Give a bounding box for every trophozoite.
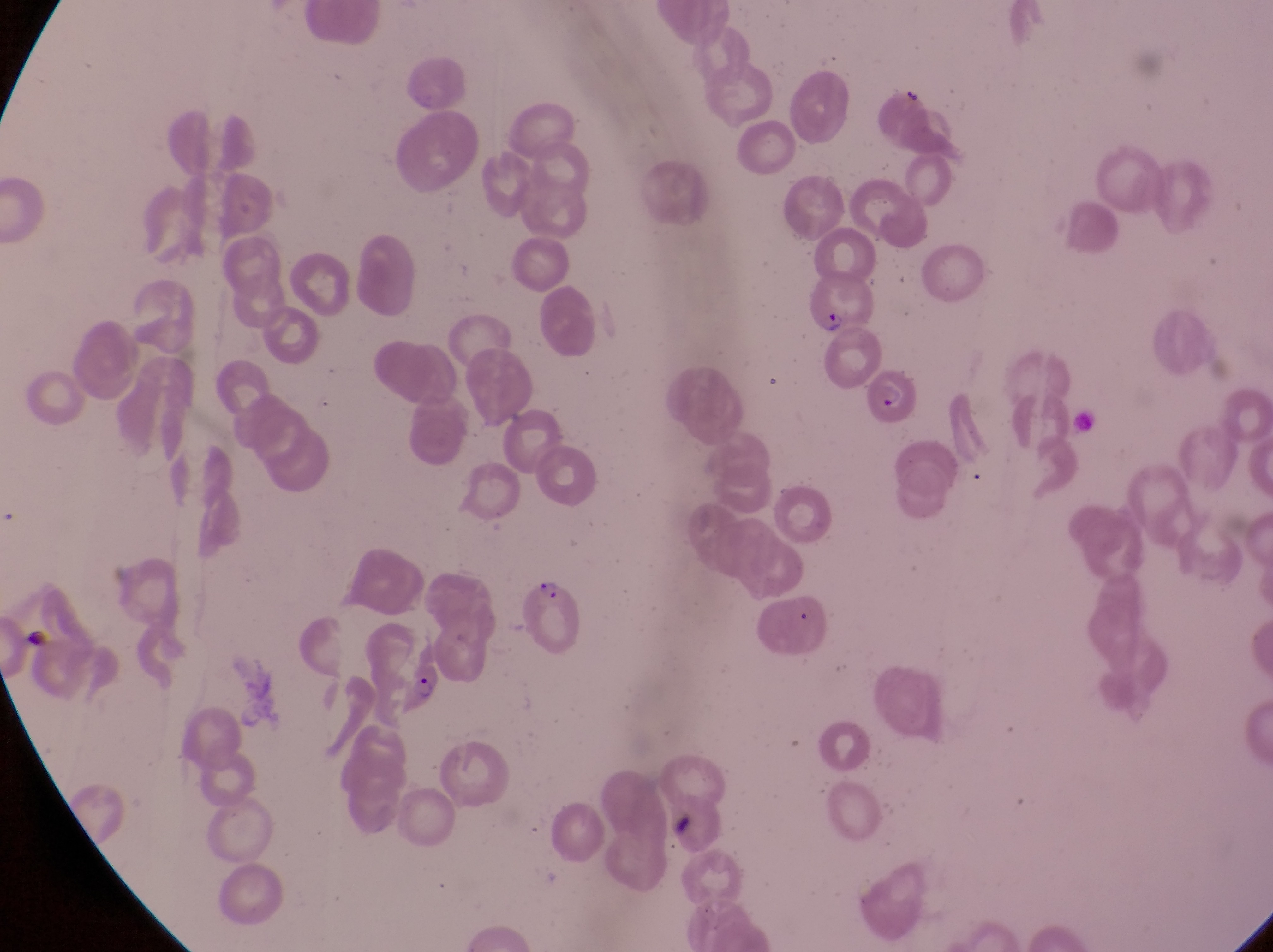
Approximate bounding boxes as [left, top, right, bottom] in pixels.
Trophozoites: [407, 674, 439, 704].

Parasitised red blood cell locations: [808, 270, 878, 335], [869, 360, 931, 430], [522, 577, 591, 654]. Single field of view. Thin blood smear. Image is 1273×952 pixels. Magnification of 1000x. Sample from Uganda. Photographed through the eyepiece of an Olympus CX-23 microscope with a smartphone camera.